Give the position of every malaria parasite.
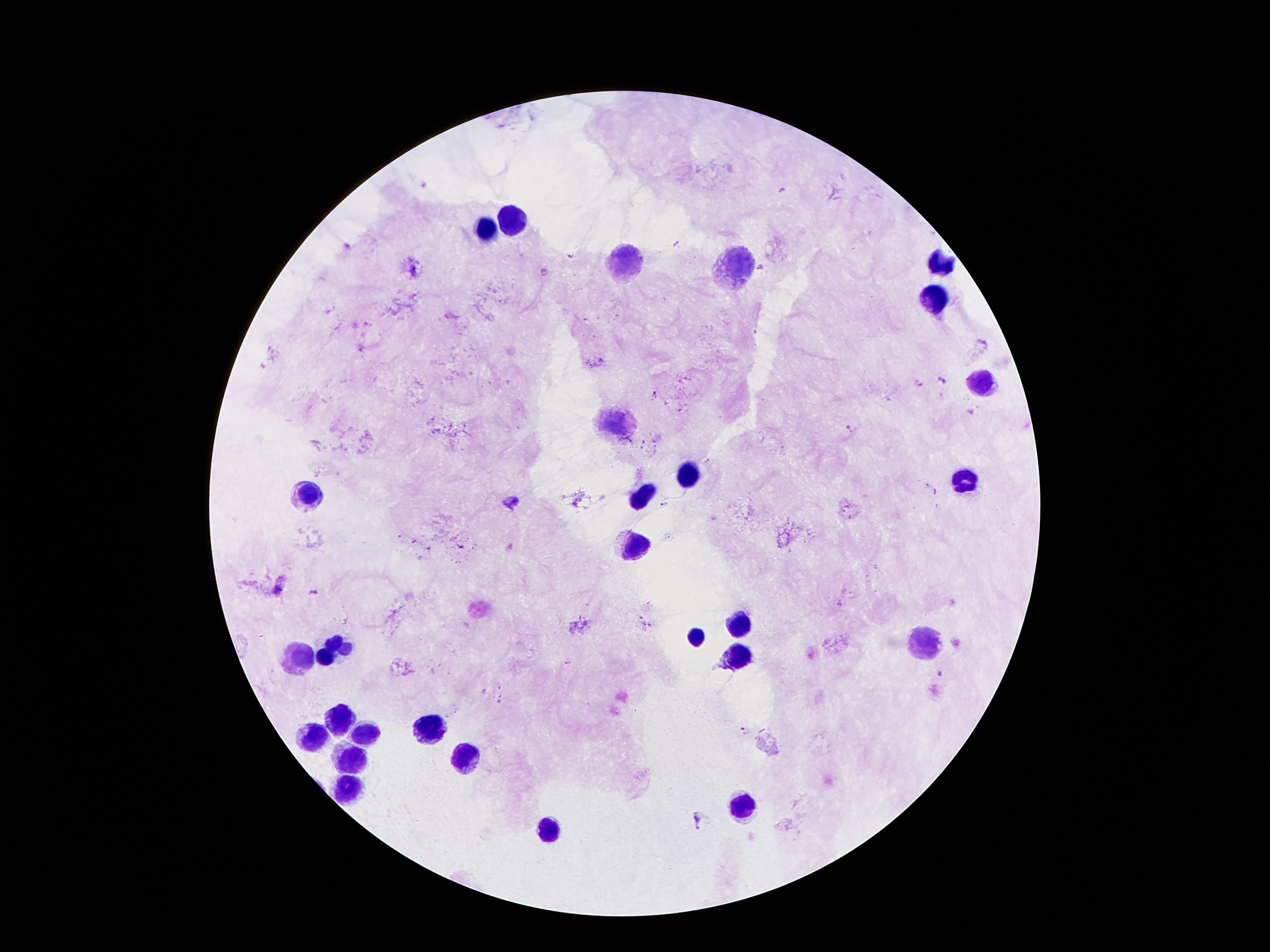
Approximate centers as (x, y) in pixels.
Malaria parasites: (571, 257), (762, 269), (942, 379), (654, 395), (850, 428), (664, 504), (277, 591), (317, 591), (940, 675), (745, 730), (699, 819).

Summary:
  - Leukocyte locations: (515, 219), (488, 229), (629, 258), (738, 265), (942, 265), (935, 300), (984, 384), (620, 422), (685, 475), (965, 483), (311, 490), (643, 496), (639, 544), (740, 624), (698, 635), (341, 638), (921, 639), (326, 654), (738, 655), (299, 658), (340, 718), (431, 728), (316, 735), (359, 735), (465, 758), (350, 760), (348, 787), (741, 807), (549, 829)
  - Magnification: 100x
  - Preparation: thick peripheral-blood smear
  - Field of view: one from this slide
  - Stain: Giemsa
  - Image size: 1270×952 pixels
  - Patient malaria status: infected with Plasmodium falciparum
  - Capture: smartphone camera through the microscope eyepiece